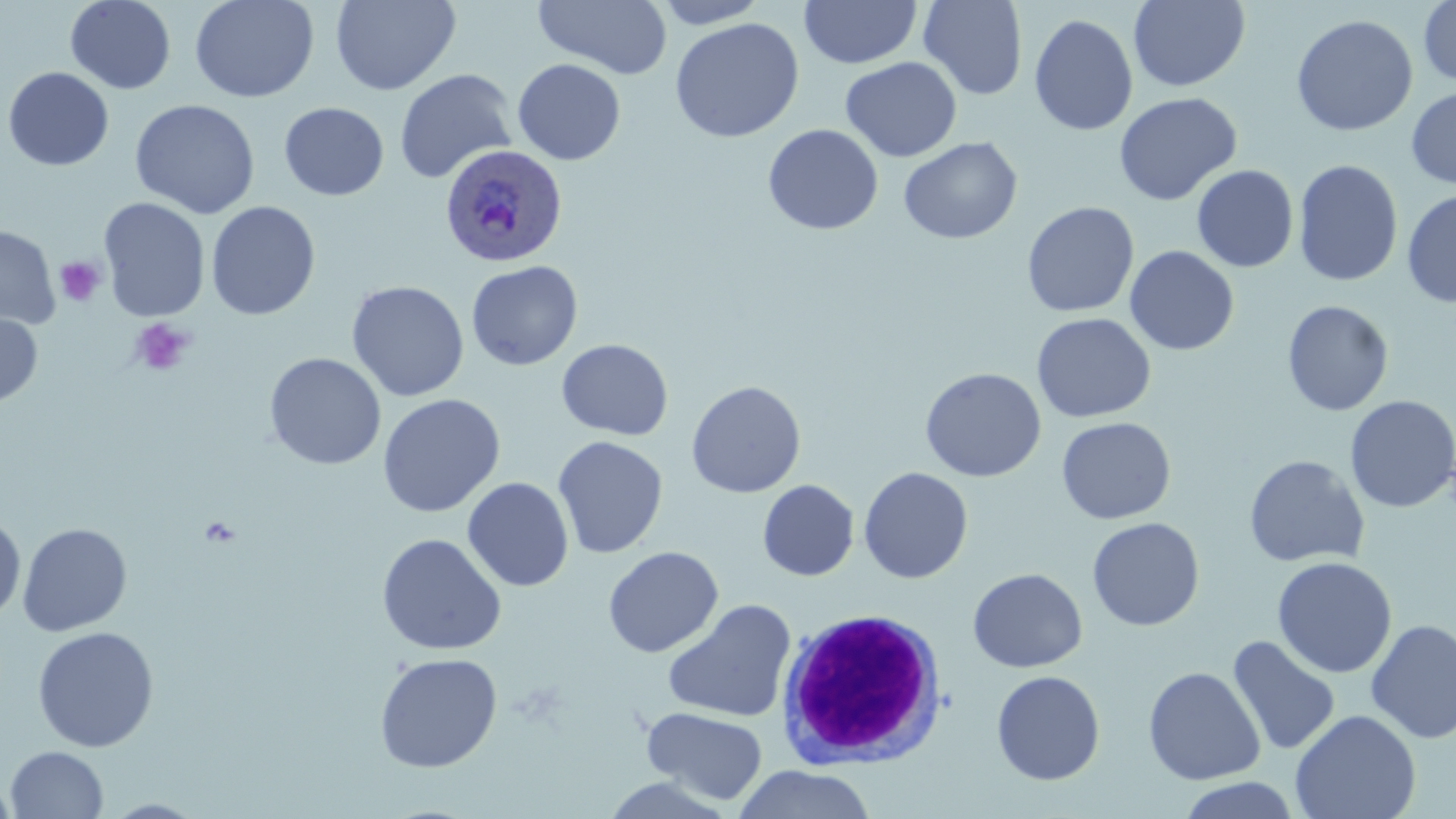
Summary:
  - Coordinate format: approximate bounding boxes as [x1, y1, x2, y2] in pixels
  - Plasmodium ovale-infected red blood cell locations: [441, 143, 569, 267]
  - Uninfected red blood cell locations: [65, 0, 177, 94], [189, 0, 319, 103], [329, 0, 461, 95], [533, 0, 674, 80], [651, 0, 771, 28], [799, 0, 922, 69], [918, 0, 1028, 100], [1128, 0, 1251, 91], [1418, 0, 1456, 87], [1029, 13, 1138, 136], [1290, 14, 1418, 136], [670, 17, 804, 143], [840, 56, 962, 162], [513, 58, 626, 165], [3, 66, 114, 171], [394, 69, 518, 184], [1406, 86, 1456, 190], [1113, 92, 1242, 206], [130, 99, 261, 219], [278, 102, 389, 201], [763, 124, 884, 235], [898, 137, 1023, 244], [1293, 159, 1403, 287], [1191, 164, 1298, 272], [1402, 189, 1456, 307], [98, 198, 211, 322], [206, 201, 320, 321], [1022, 201, 1139, 318], [0, 225, 60, 331], [1124, 245, 1239, 356], [466, 260, 583, 371], [346, 280, 469, 402], [1282, 300, 1394, 416], [0, 311, 42, 408], [1031, 312, 1156, 423], [556, 339, 673, 440], [264, 353, 387, 470], [920, 367, 1046, 482], [686, 380, 806, 498], [377, 393, 505, 518], [1344, 395, 1456, 514], [1056, 417, 1176, 524], [552, 436, 668, 559], [1244, 454, 1370, 568], [858, 466, 973, 583], [462, 477, 574, 592], [758, 479, 859, 581], [0, 516, 26, 623], [1087, 517, 1205, 631], [17, 522, 132, 637], [376, 533, 507, 655], [602, 546, 723, 657], [1272, 556, 1397, 679], [967, 567, 1087, 672], [662, 599, 797, 723], [1365, 619, 1456, 744], [32, 626, 159, 752], [1227, 635, 1341, 757], [374, 652, 503, 773], [1142, 666, 1265, 785], [991, 670, 1106, 785], [642, 707, 768, 805], [1290, 709, 1421, 819], [6, 746, 109, 819], [734, 765, 876, 819], [595, 775, 735, 818], [0, 776, 18, 819], [1175, 777, 1302, 818], [100, 799, 209, 818]
  - Platelet locations: [55, 256, 106, 307], [130, 318, 195, 377]
  - White blood cell locations: [776, 607, 949, 770]
  - Slide-level diagnosis: Plasmodium ovale
  - Magnification: 1000x
  - Modality: optical microscopy
  - Field of view: one of a larger specimen
  - Preparation: thin blood smear
  - Stain: May-Grünwald-Giemsa
  - Image size: 1456×819 pixels